Give the extent of all uninfected red blood cells.
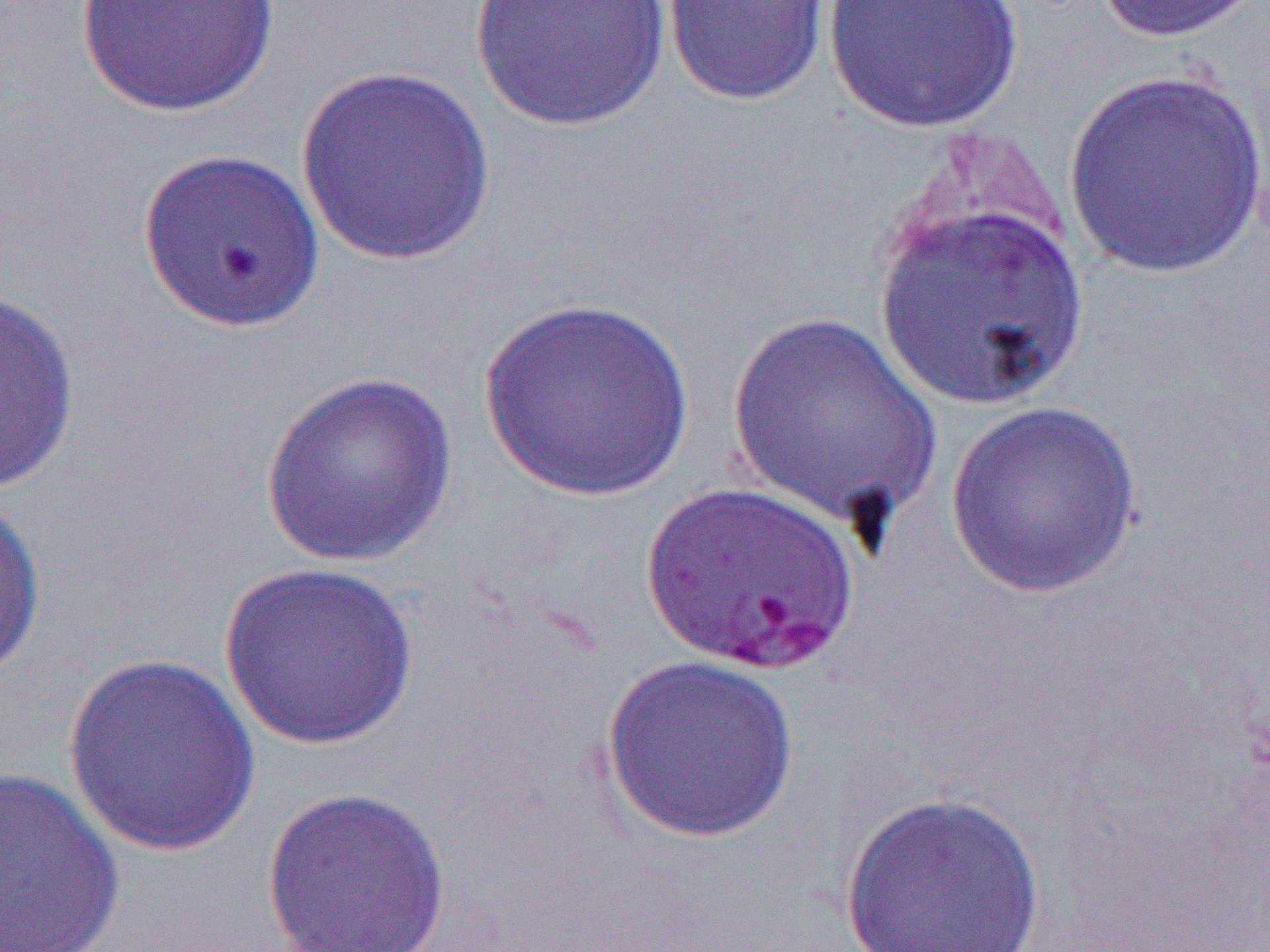

Approximate bounding boxes as [x1, y1, x2, y2] in pixels.
Uninfected red blood cells: [74, 0, 281, 118], [469, 0, 672, 133], [661, 0, 833, 107], [822, 0, 1025, 135], [1090, 0, 1267, 44], [295, 66, 497, 266], [1062, 71, 1270, 277], [137, 147, 325, 334], [874, 194, 1089, 411], [0, 287, 80, 495], [479, 296, 695, 501], [727, 311, 943, 532], [259, 370, 458, 569], [944, 400, 1144, 598], [0, 488, 45, 686], [219, 562, 420, 751], [62, 653, 263, 857], [600, 653, 801, 843], [0, 767, 125, 951], [259, 784, 452, 952], [840, 789, 1047, 951].

Slide-level diagnosis: Plasmodium falciparum. Optical microscopy. One field of a larger specimen. Image is 1270×952 pixels. Captured at 1000x magnification. Thin blood film.